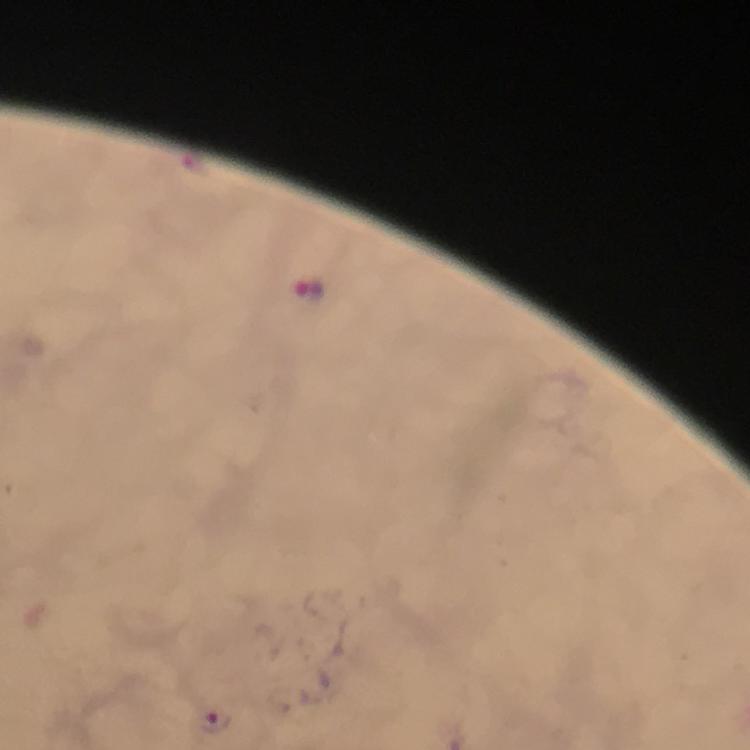 Approximate centers as {x, y} in pixels. Malaria parasite locations: {217, 722}. Thick blood film. 100x magnification. From a diagnostic examination for malaria. Giemsa-stained preparation. Image is 750×750 pixels. A crop from one field of view. Immersion oil was used. Photographed through the microscope with a smartphone camera.